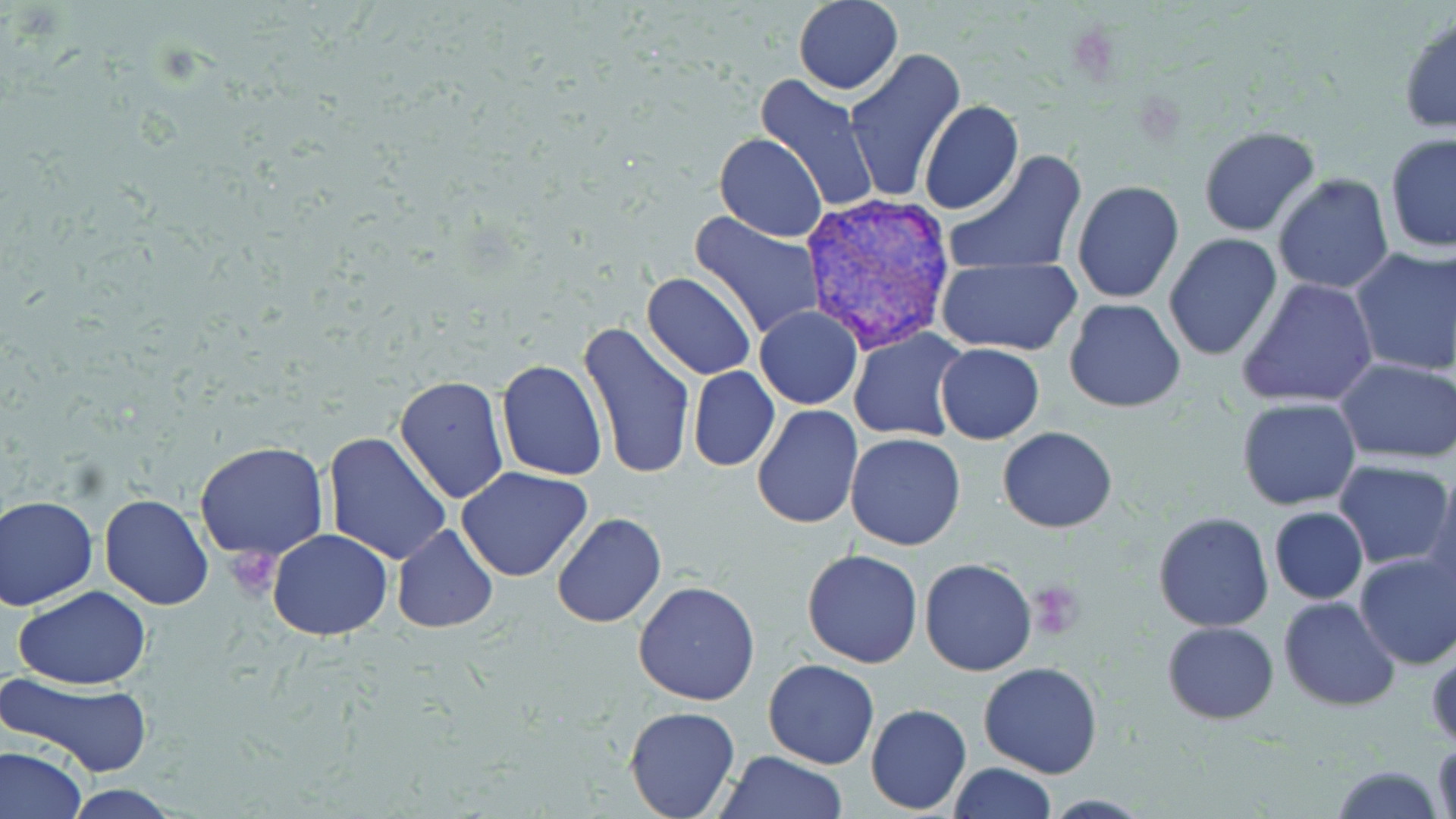 Approximate bounding boxes as named x1/y1/x2/y2 corners in pixels. Platelet locations: (x1=226, y1=546, x2=282, y2=597), (x1=1032, y1=578, x2=1086, y2=636). Uninfected red blood cell locations: (x1=794, y1=0, x2=902, y2=94), (x1=1399, y1=15, x2=1456, y2=135), (x1=842, y1=50, x2=965, y2=203), (x1=754, y1=74, x2=879, y2=216), (x1=919, y1=101, x2=1023, y2=217), (x1=1198, y1=125, x2=1323, y2=238), (x1=714, y1=132, x2=827, y2=241), (x1=1383, y1=133, x2=1456, y2=254), (x1=944, y1=152, x2=1087, y2=277), (x1=1272, y1=173, x2=1396, y2=293), (x1=1071, y1=179, x2=1185, y2=303), (x1=689, y1=211, x2=826, y2=341), (x1=1163, y1=234, x2=1283, y2=361), (x1=1349, y1=245, x2=1456, y2=379), (x1=935, y1=257, x2=1081, y2=355), (x1=642, y1=272, x2=758, y2=379), (x1=1237, y1=276, x2=1379, y2=411), (x1=1063, y1=299, x2=1187, y2=414), (x1=754, y1=305, x2=862, y2=410), (x1=578, y1=319, x2=696, y2=483), (x1=849, y1=327, x2=967, y2=442), (x1=935, y1=343, x2=1044, y2=444), (x1=1336, y1=357, x2=1456, y2=463), (x1=497, y1=359, x2=608, y2=481), (x1=687, y1=365, x2=780, y2=472), (x1=394, y1=375, x2=509, y2=506), (x1=1237, y1=398, x2=1360, y2=510), (x1=751, y1=406, x2=864, y2=530), (x1=997, y1=426, x2=1118, y2=533), (x1=322, y1=431, x2=454, y2=566), (x1=846, y1=434, x2=965, y2=551), (x1=192, y1=441, x2=331, y2=562), (x1=1334, y1=460, x2=1452, y2=569), (x1=457, y1=465, x2=592, y2=582), (x1=1424, y1=472, x2=1456, y2=603), (x1=99, y1=493, x2=214, y2=609), (x1=1, y1=495, x2=98, y2=610), (x1=1268, y1=507, x2=1367, y2=605), (x1=551, y1=512, x2=667, y2=628), (x1=1153, y1=512, x2=1274, y2=631), (x1=392, y1=524, x2=498, y2=634), (x1=267, y1=530, x2=394, y2=641), (x1=802, y1=549, x2=923, y2=668), (x1=1353, y1=549, x2=1456, y2=669), (x1=919, y1=557, x2=1036, y2=676), (x1=1312, y1=578, x2=1448, y2=697), (x1=633, y1=579, x2=761, y2=706), (x1=13, y1=586, x2=152, y2=689), (x1=1278, y1=596, x2=1400, y2=711), (x1=1162, y1=621, x2=1279, y2=724), (x1=1428, y1=649, x2=1455, y2=750), (x1=763, y1=658, x2=881, y2=769), (x1=978, y1=661, x2=1103, y2=779), (x1=3, y1=672, x2=155, y2=776), (x1=623, y1=704, x2=741, y2=819), (x1=866, y1=704, x2=971, y2=814), (x1=1432, y1=737, x2=1454, y2=819), (x1=0, y1=746, x2=85, y2=818), (x1=718, y1=750, x2=846, y2=819), (x1=946, y1=762, x2=1057, y2=819), (x1=1330, y1=763, x2=1447, y2=819), (x1=61, y1=785, x2=184, y2=818). Plasmodium vivax-infected red blood cell locations: (x1=803, y1=196, x2=954, y2=352). Slide-level diagnosis: Plasmodium vivax. One field of a larger specimen. May-Grünwald-Giemsa-stained preparation. Image is 1456×819 pixels. 1000x magnification. Optical microscopy. Thin blood film.